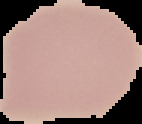

image_size: 142×124 pixels
preparation: thin blood film
image_type: segmented cell region on a black background
malaria_status: uninfected